Identify the blood parasite species.
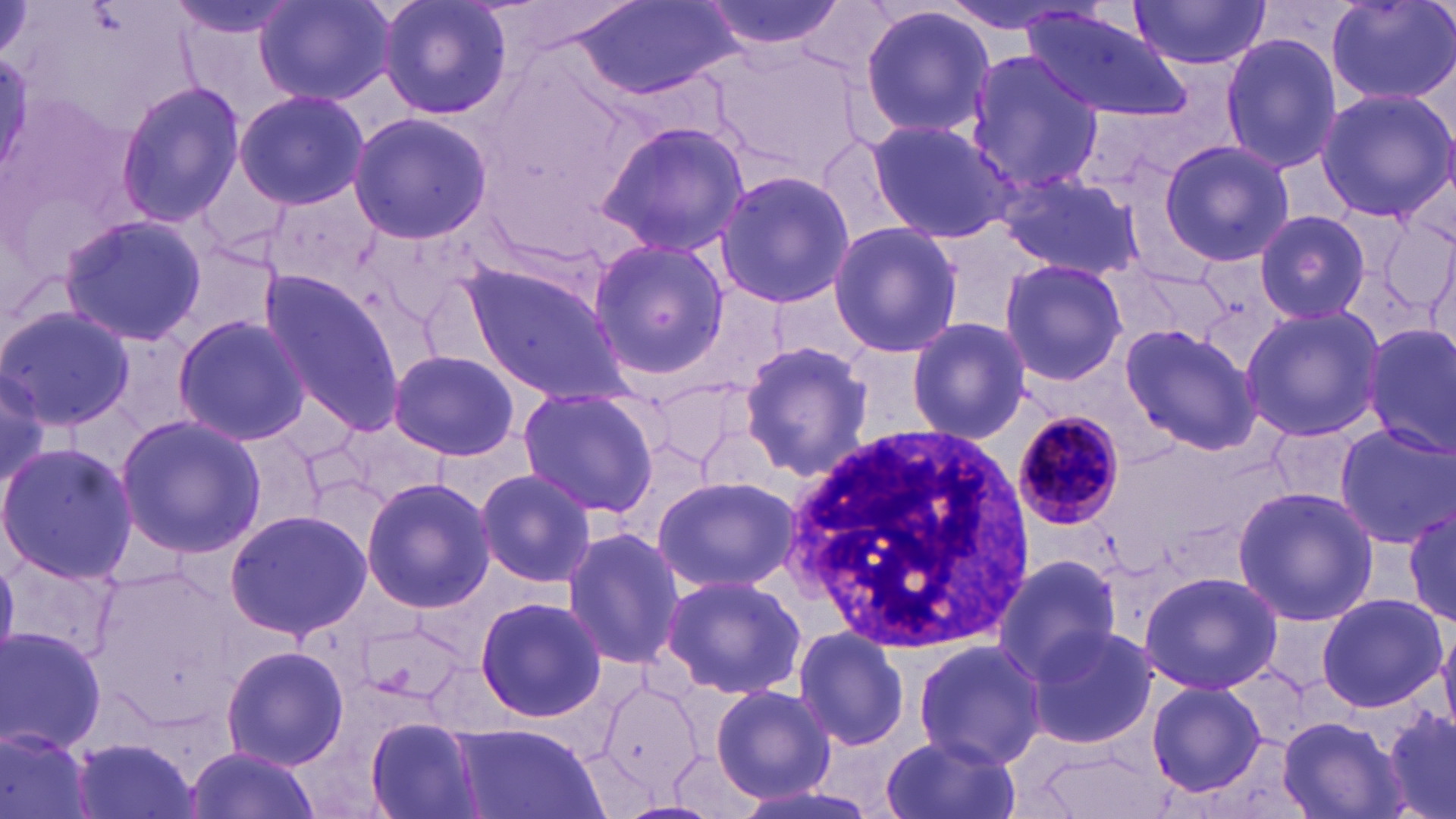
Plasmodium malariae.

Approximate bounding boxes as [x1, y1, x2, y2] in pixels. White blood cell locations: [785, 417, 1036, 652]. Plasmodium malariae-infected red blood cell locations: [1010, 408, 1127, 533]. Uninfected red blood cell locations: [254, 0, 394, 105], [375, 0, 514, 122], [571, 0, 735, 102], [698, 0, 850, 56], [933, 0, 1105, 38], [1327, 0, 1455, 107], [1128, 1, 1272, 70], [858, 5, 995, 141], [1021, 9, 1189, 120], [1219, 32, 1346, 177], [961, 51, 1101, 199], [114, 81, 247, 231], [1315, 87, 1456, 223], [233, 89, 370, 209], [346, 112, 493, 246], [865, 119, 1015, 244], [595, 120, 751, 255], [817, 135, 916, 250], [1157, 137, 1294, 269], [193, 155, 294, 260], [714, 169, 854, 311], [995, 170, 1144, 279], [1254, 208, 1374, 324], [58, 214, 211, 349], [827, 222, 963, 359], [587, 238, 730, 381], [997, 259, 1129, 388], [461, 262, 635, 407], [1127, 269, 1235, 347], [256, 272, 407, 435], [418, 280, 509, 369], [0, 304, 136, 430], [1240, 305, 1388, 442], [171, 313, 311, 447], [905, 316, 1031, 445], [1120, 322, 1259, 455], [1361, 323, 1456, 458], [737, 339, 874, 479], [389, 350, 519, 459], [0, 364, 54, 495], [516, 386, 663, 516], [115, 413, 265, 558], [337, 418, 450, 502], [1265, 420, 1364, 507], [1334, 422, 1454, 546], [0, 443, 138, 583], [475, 469, 596, 589], [653, 475, 800, 593], [360, 477, 495, 612], [599, 485, 780, 636], [1232, 485, 1379, 627], [1402, 505, 1455, 628], [224, 509, 372, 641], [561, 528, 686, 669], [3, 549, 122, 670], [992, 552, 1124, 681], [1138, 570, 1283, 695], [659, 573, 808, 700], [1315, 592, 1448, 714], [472, 595, 606, 722], [1437, 618, 1456, 733], [1024, 624, 1158, 750], [0, 625, 109, 753], [791, 625, 911, 752], [911, 640, 1047, 767], [219, 644, 349, 771], [1146, 679, 1268, 797], [710, 682, 836, 805], [1381, 708, 1456, 819], [1277, 713, 1406, 819], [364, 716, 484, 819], [450, 723, 603, 819], [0, 726, 95, 819], [881, 731, 1020, 819], [65, 736, 203, 819], [670, 745, 763, 819], [182, 747, 316, 819], [725, 776, 888, 819]. Image is 1456×819 pixels. One field of a larger specimen. May-Grünwald-Giemsa stain. 1000x magnification. Optical microscopy. Thin blood smear.